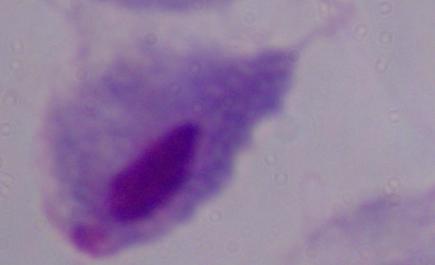
identification = trichomonad
modality = micrograph
magnification = 1000x